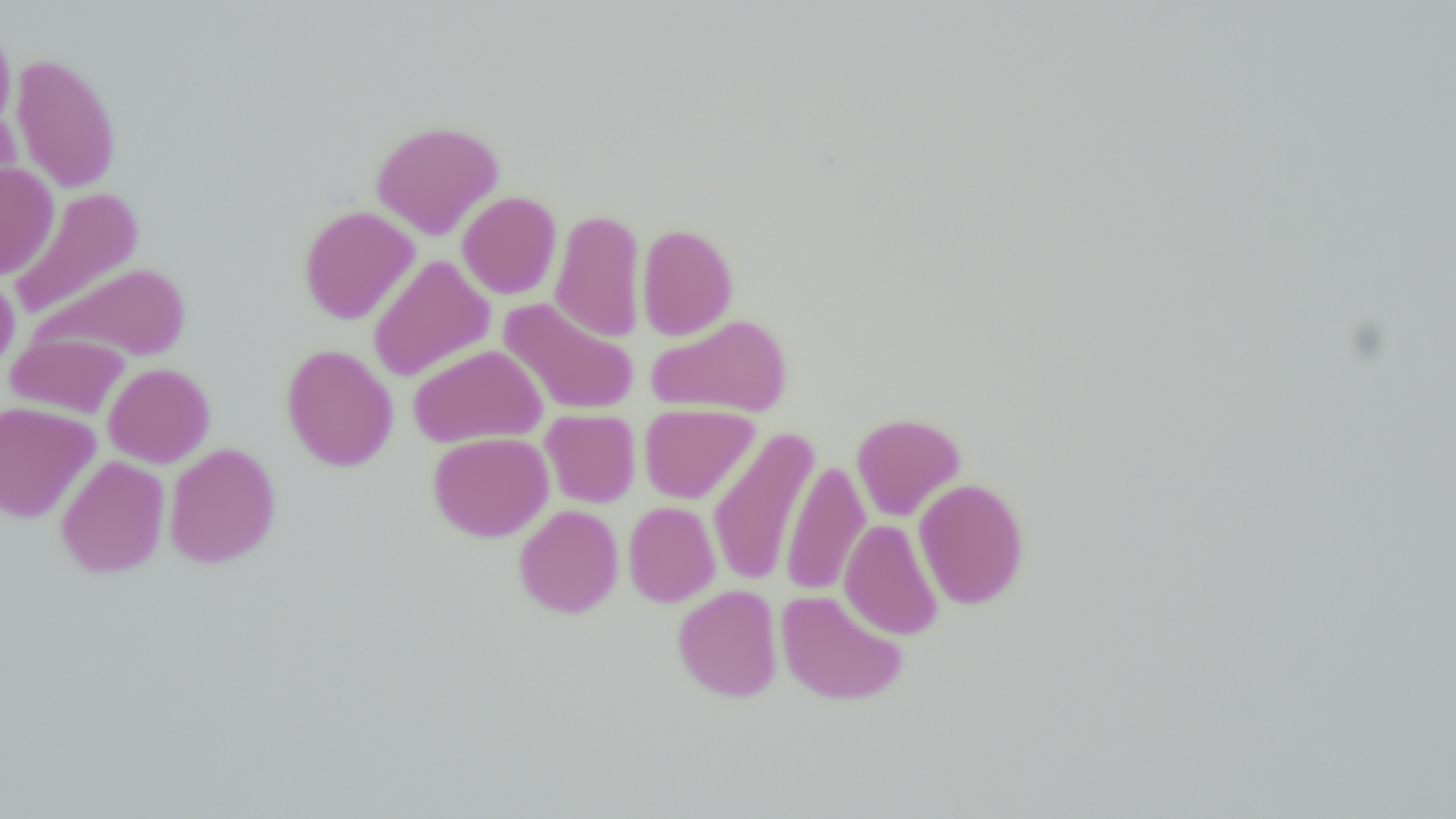

Summary:
  - Coordinate format: approximate bounding boxes as [x1, y1, x2, y2] in pixels
  - Uninfected red blood cell locations: [0, 21, 16, 138], [10, 53, 121, 193], [0, 106, 22, 214], [370, 119, 504, 240], [0, 162, 60, 279], [9, 186, 145, 321], [457, 191, 562, 299], [298, 205, 420, 325], [549, 208, 647, 343], [636, 223, 738, 340], [368, 254, 496, 382], [33, 262, 192, 362], [0, 269, 20, 378], [498, 297, 640, 416], [647, 313, 793, 418], [6, 333, 130, 419], [280, 343, 399, 472], [408, 343, 547, 447], [103, 362, 215, 468], [0, 401, 101, 523], [639, 403, 759, 504], [540, 409, 641, 508], [851, 413, 966, 522], [707, 427, 819, 587], [427, 432, 554, 542], [164, 442, 281, 568], [56, 455, 170, 578], [782, 460, 870, 597], [914, 478, 1030, 610], [623, 501, 721, 607], [513, 504, 624, 619], [839, 518, 944, 640], [672, 584, 783, 702], [775, 589, 908, 706]
  - Slide-level diagnosis: no evidence of blood parasites
  - Preparation: thin blood film
  - Modality: optical microscopy
  - Magnification: 1000x
  - Field of view: one of a larger specimen
  - Image size: 1456×819 pixels